Assess this cell for malaria.
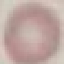
Uninfected.

Cell patch, automatically extracted from a larger field of view and resized to 64 × 64 pixels. Thin smear of blood. Acquired by smartphone through the microscope eyepiece. Giemsa stain.